Point out each Plasmodium parasite.
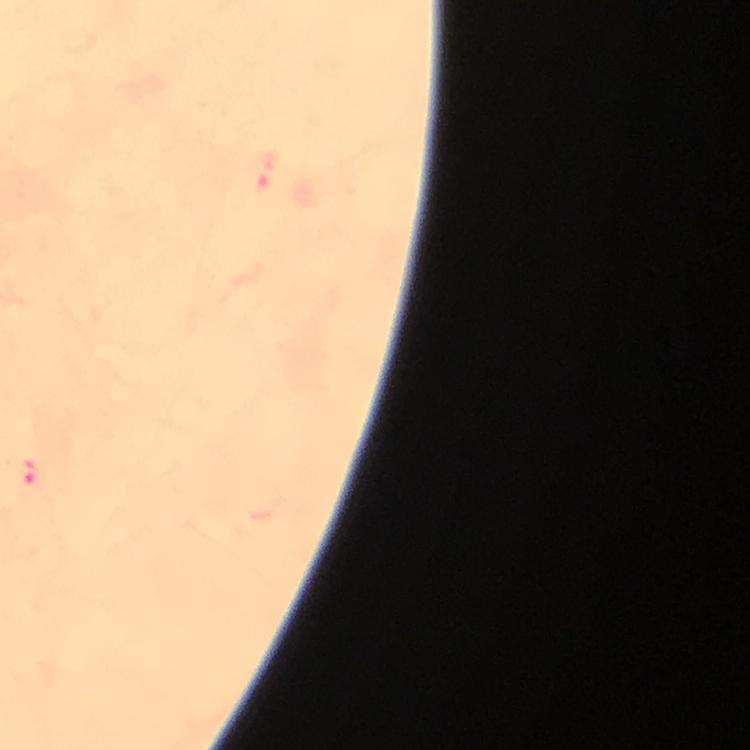

Approximate centers as [x, y] in pixels.
Plasmodium parasites: [29, 476].

Summary:
  - Stain: Giemsa
  - Cropped from: a single field of view
  - Magnification: 100x
  - Preparation: thick blood smear
  - Capture: smartphone camera through the microscope
  - Context: from a diagnostic examination for malaria
  - Immersion oil: used
  - Image size: 750×750 pixels